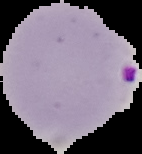
Summary:
  - Image size: 142×154 pixels
  - Result: Plasmodium parasites identified
  - Preparation: thin blood smear
  - Image type: cell region segmented out of the field of view; surrounding area masked to black